Comment on the morphology of the erythrocytes.
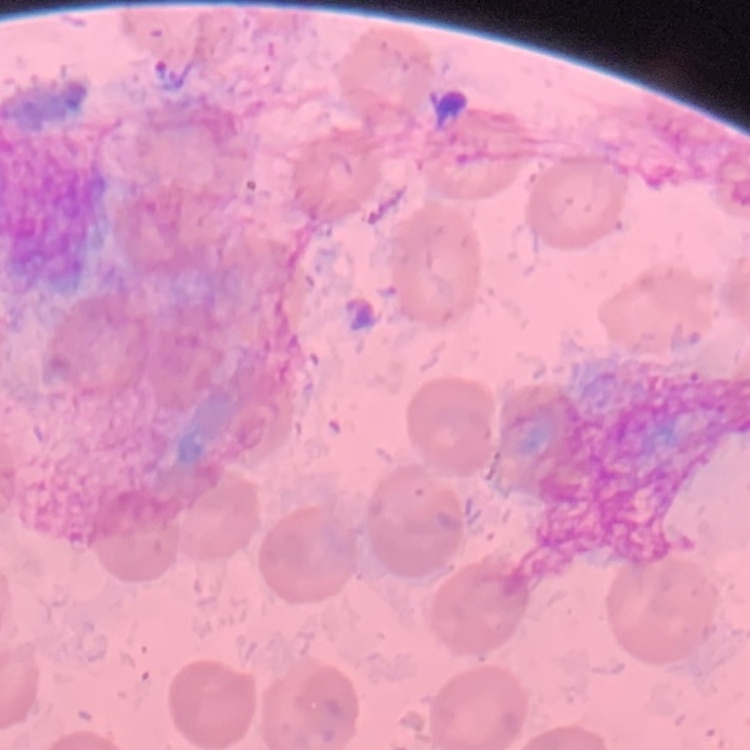
They show no rouleaux formation.

image type = square crop of a larger photomicrograph
stain = Field's or Giemsa
preparation = thin blood smear